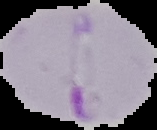
From a thin blood film. Cell region segmented out of the field of view; the surrounding area is masked to black. Malaria status: parasitized. Image is 157×130 pixels.